Identify the parasite.
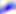

This is Toxoplasma gondii.

Micrograph. Captured at 400x magnification.